Assess for parasitized red blood cells.
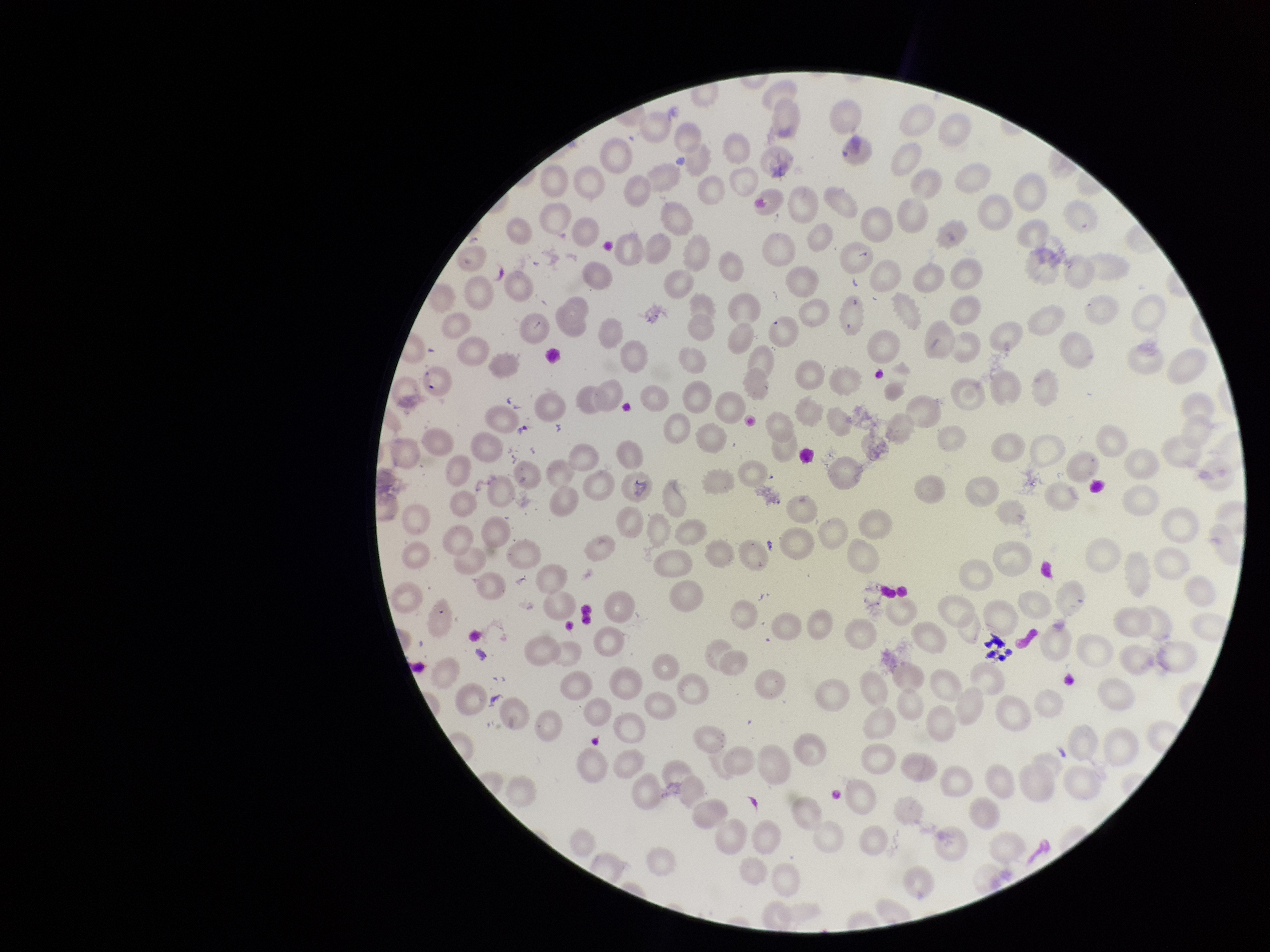

None detected.

{
  "preparation": "thin smear",
  "parasitized_red_blood_cell_count": 0,
  "image_size": "1270×952 pixels",
  "species_reported_for_this_patient": "Plasmodium falciparum",
  "stain": "Giemsa",
  "capture": "smartphone photograph through the microscope eyepiece",
  "red_blood_cell_count": 177,
  "field_of_view": "one from this slide",
  "patient_malaria_status": "infected"
}